Describe the morphology of the erythrocytes.
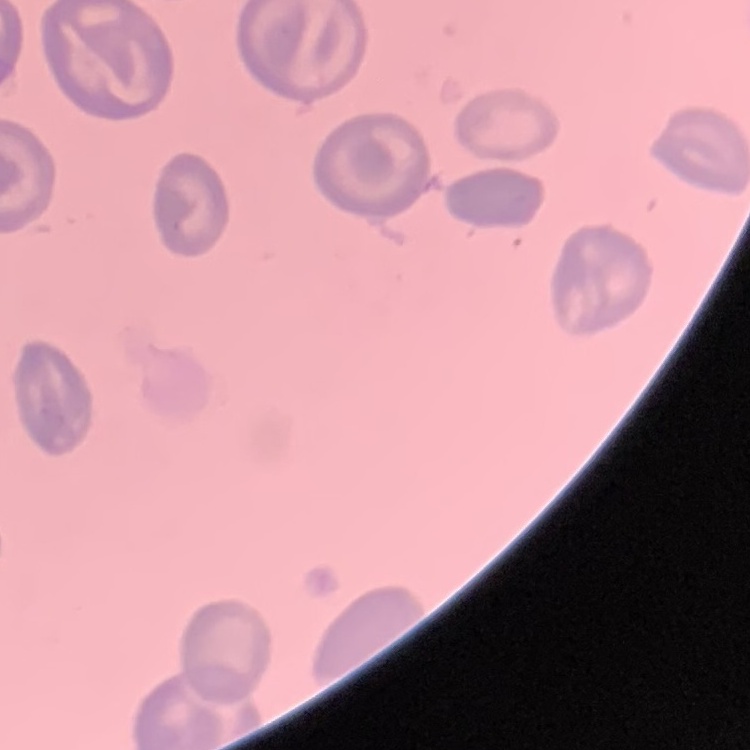
They show no rouleaux formation.

Summary:
  - Image type: square crop of a larger photomicrograph
  - Stain: Field's or Giemsa
  - Preparation: thin blood film